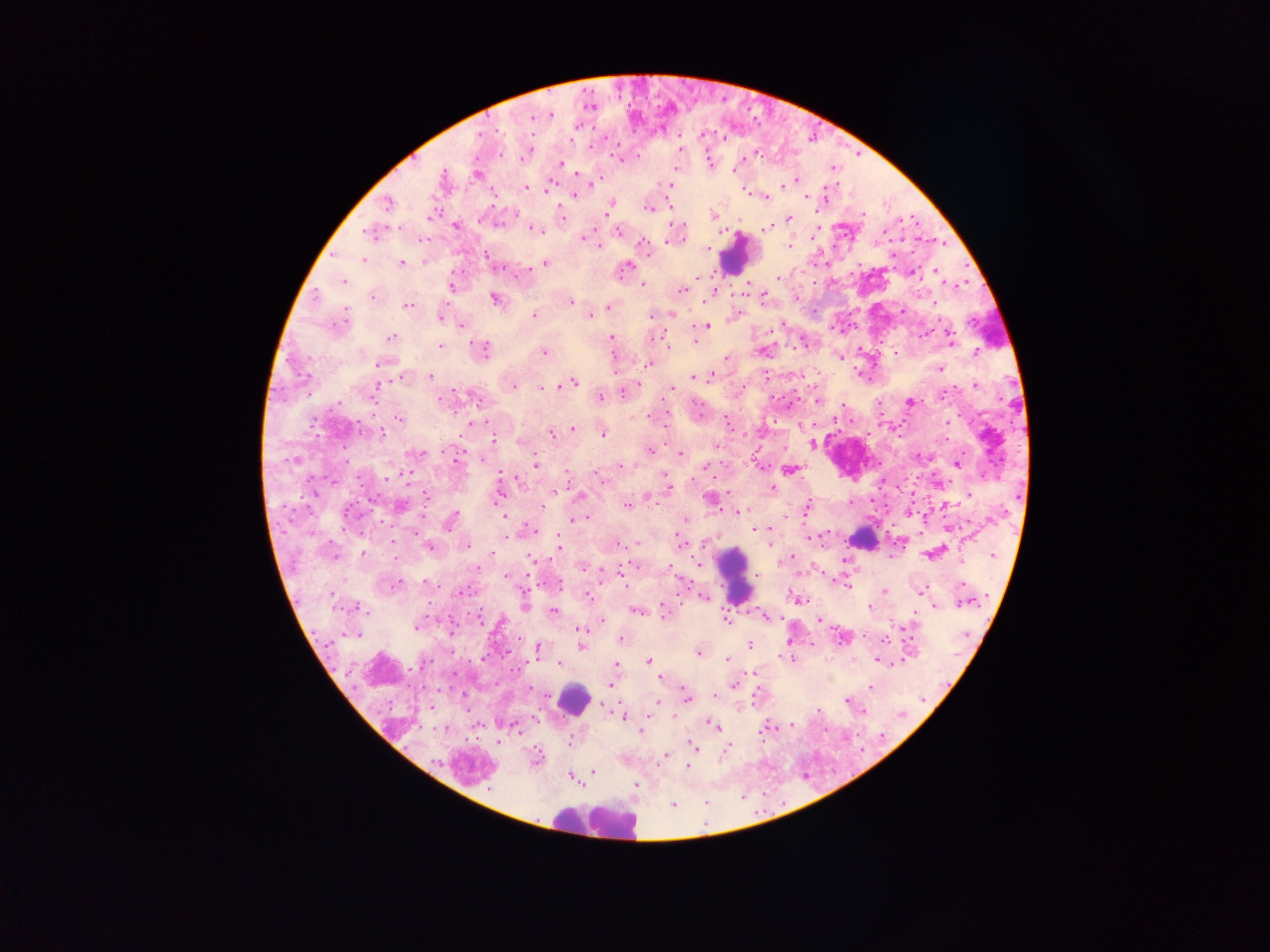 Approximate centers as [x, y] in pixels. Leukocyte locations: [735, 254], [865, 542], [735, 575], [572, 698], [594, 822]. Malaria parasite locations: [551, 115], [532, 118], [679, 149], [527, 153], [621, 159], [559, 162], [709, 162], [676, 167], [476, 175], [442, 179], [796, 179], [550, 182], [593, 184], [784, 185], [526, 187], [547, 188], [669, 188], [750, 193], [574, 195], [766, 196], [805, 197], [824, 198], [387, 203], [610, 207], [648, 207], [713, 214], [563, 218], [789, 219], [456, 226], [768, 228], [533, 229], [618, 231], [371, 232], [584, 239], [789, 245], [706, 250], [487, 257], [363, 259], [491, 261], [401, 263], [544, 263], [626, 266], [910, 273], [936, 273], [777, 276], [342, 281], [451, 285], [642, 285], [683, 289], [713, 291], [371, 296], [495, 298], [762, 299], [570, 302], [933, 304], [408, 305], [609, 306], [903, 311], [671, 313], [534, 315], [590, 315], [651, 315], [440, 316], [735, 316], [342, 320], [460, 324], [782, 324], [707, 326], [612, 337], [653, 337], [391, 338], [950, 339], [695, 341], [668, 345], [440, 346], [482, 349], [544, 351], [763, 351], [975, 352], [612, 356], [840, 357], [727, 359], [382, 363], [649, 364], [939, 368], [401, 376], [430, 376], [694, 376], [711, 376], [572, 382], [975, 385], [375, 386], [512, 386], [671, 388], [543, 389], [623, 391], [373, 393], [599, 397], [441, 399], [816, 399], [911, 402], [837, 417], [400, 418], [664, 422], [471, 423], [947, 423], [572, 429], [380, 430], [551, 433], [603, 434], [493, 438], [812, 443], [717, 445], [649, 451], [416, 453], [680, 454], [481, 459], [956, 463], [535, 464], [620, 466], [789, 469], [567, 474], [601, 479], [771, 487], [668, 489], [499, 490], [968, 494], [579, 495], [426, 497], [648, 498], [710, 498], [399, 505], [544, 505], [627, 505], [807, 507], [944, 507], [909, 511], [348, 512], [739, 513], [503, 516], [583, 517], [781, 517], [684, 518], [574, 519], [450, 521], [949, 528], [755, 529], [534, 530], [507, 534], [809, 537], [636, 542], [393, 543], [681, 543], [770, 543], [428, 546], [466, 546], [558, 547], [492, 553], [934, 553], [362, 554], [992, 554], [530, 557], [788, 558], [582, 565], [632, 565], [699, 566], [670, 567], [477, 569], [755, 575], [506, 576], [425, 582], [558, 584], [396, 585], [845, 585], [883, 590], [460, 591], [920, 591], [587, 595], [702, 597], [797, 598], [964, 601], [524, 604], [933, 605], [355, 606], [868, 607], [637, 611], [553, 612], [665, 612], [764, 615], [725, 618], [480, 619], [820, 620], [601, 621], [416, 626], [579, 630], [843, 637], [884, 639], [621, 640], [749, 644], [580, 646], [536, 649], [698, 652], [790, 658], [648, 661], [728, 661], [880, 661], [559, 662], [896, 662], [615, 664], [755, 672], [661, 678], [734, 684], [611, 685], [870, 686], [715, 694], [465, 695], [684, 698], [847, 700], [654, 702], [601, 704], [431, 707], [622, 716], [645, 717], [790, 724], [714, 726], [766, 726], [517, 729], [641, 731], [570, 740], [691, 746], [726, 748], [665, 756], [536, 758], [686, 766], [593, 771], [569, 776], [636, 784], [672, 805]. Collected in Ghana. Single field of view. Thick blood smear. Photographed through a microscope with a mobile-phone camera. Image is 1270×952 pixels.